Comment on the morphology of the red blood cells.
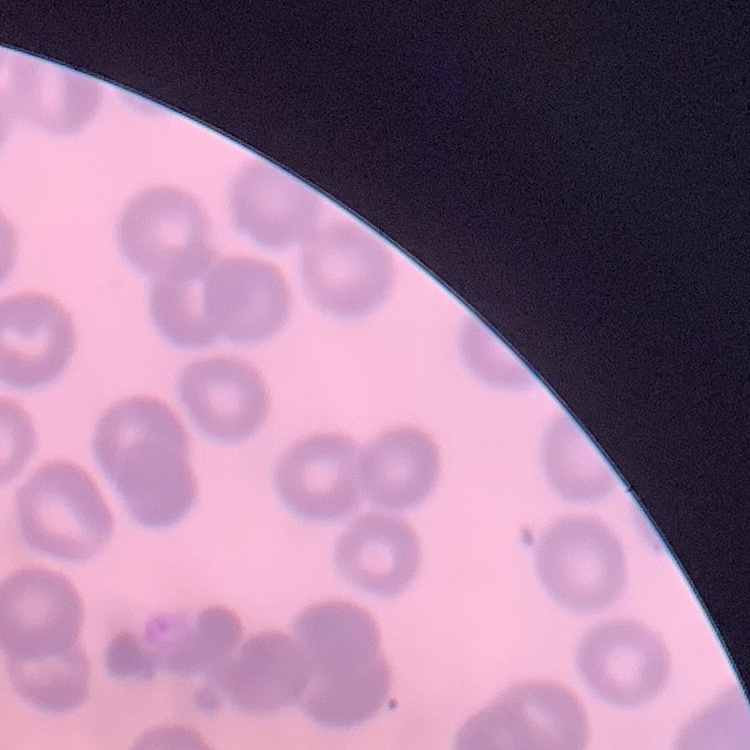

They show no rouleaux formation.

Summary:
  - Image type: square crop of a larger photomicrograph
  - Preparation: thin peripheral smear
  - Stain: Field's or Giemsa